State which parasite is depicted.
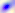
Toxoplasma gondii.

Photomicrograph. Captured at 400x magnification.